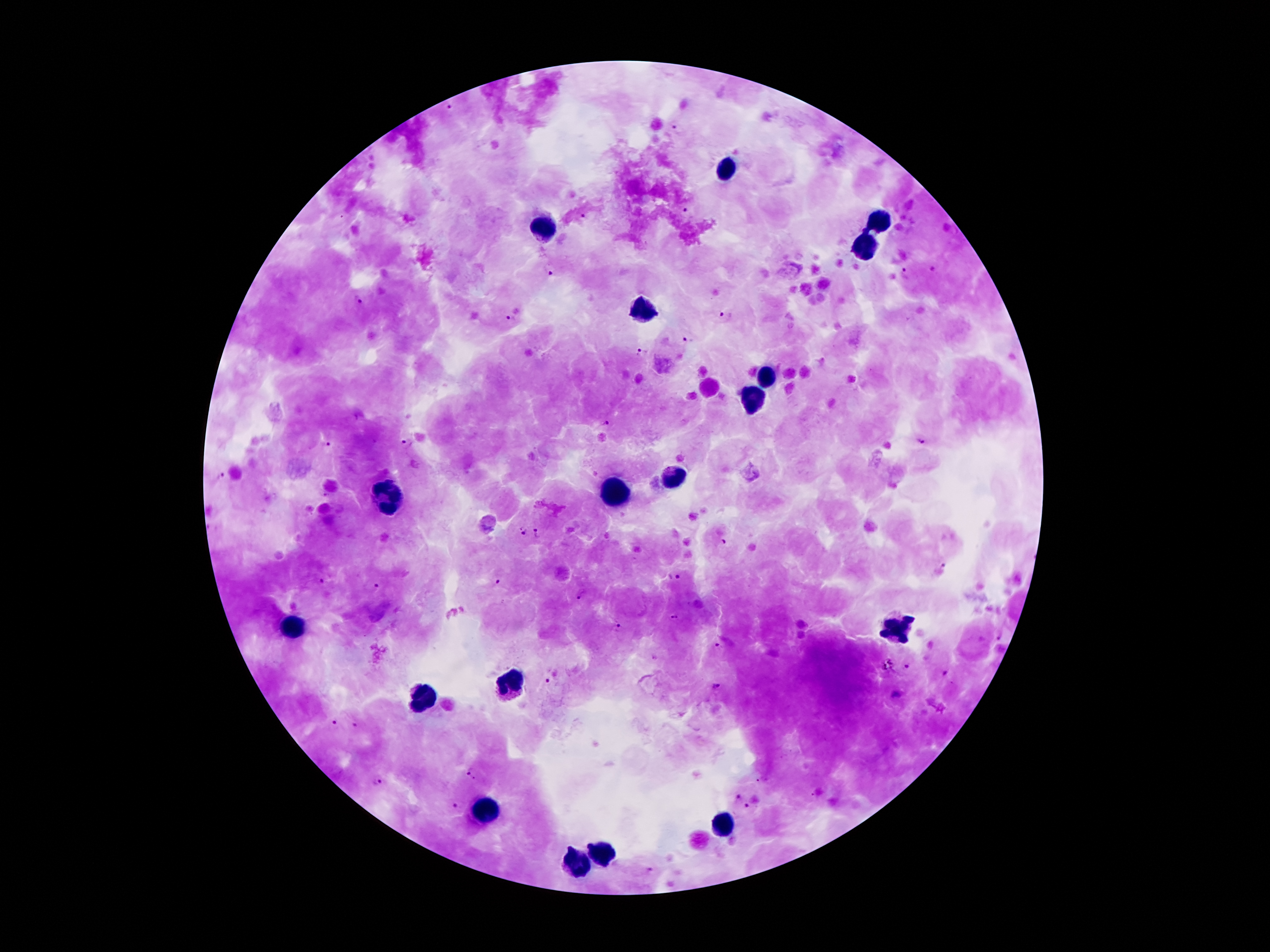
{
  "stain": "Giemsa",
  "capture": "smartphone camera through the microscope eyepiece",
  "preparation": "thick blood film",
  "plasmodium_parasite_locations": "approximate object centers, in pixels from the top-left corner: (x=446, y=105), (x=676, y=127), (x=685, y=211), (x=580, y=219), (x=933, y=266), (x=550, y=270), (x=906, y=273), (x=356, y=300), (x=510, y=316), (x=724, y=317), (x=686, y=339), (x=640, y=354), (x=605, y=423), (x=922, y=442), (x=407, y=443), (x=325, y=445), (x=220, y=477), (x=522, y=530), (x=539, y=533), (x=723, y=541), (x=942, y=565), (x=674, y=576), (x=499, y=581), (x=319, y=582), (x=374, y=586), (x=579, y=598), (x=675, y=618), (x=615, y=625), (x=998, y=639), (x=720, y=644), (x=904, y=665), (x=944, y=674), (x=548, y=681), (x=715, y=688), (x=333, y=722), (x=357, y=724), (x=472, y=773), (x=377, y=780), (x=737, y=795), (x=457, y=803), (x=748, y=807), (x=648, y=872)",
  "magnification": "100x",
  "leukocyte_locations": "approximate object centers, in pixels from the top-left corner: (x=726, y=170), (x=882, y=219), (x=547, y=228), (x=866, y=248), (x=644, y=311), (x=763, y=380), (x=754, y=397), (x=673, y=475), (x=612, y=497), (x=386, y=499), (x=898, y=625), (x=290, y=626), (x=511, y=685), (x=427, y=692), (x=486, y=809), (x=722, y=821), (x=602, y=854), (x=574, y=863)",
  "patient_malaria_status": "infected with Plasmodium falciparum",
  "field_of_view": "single",
  "image_size": "1270×952 pixels"
}